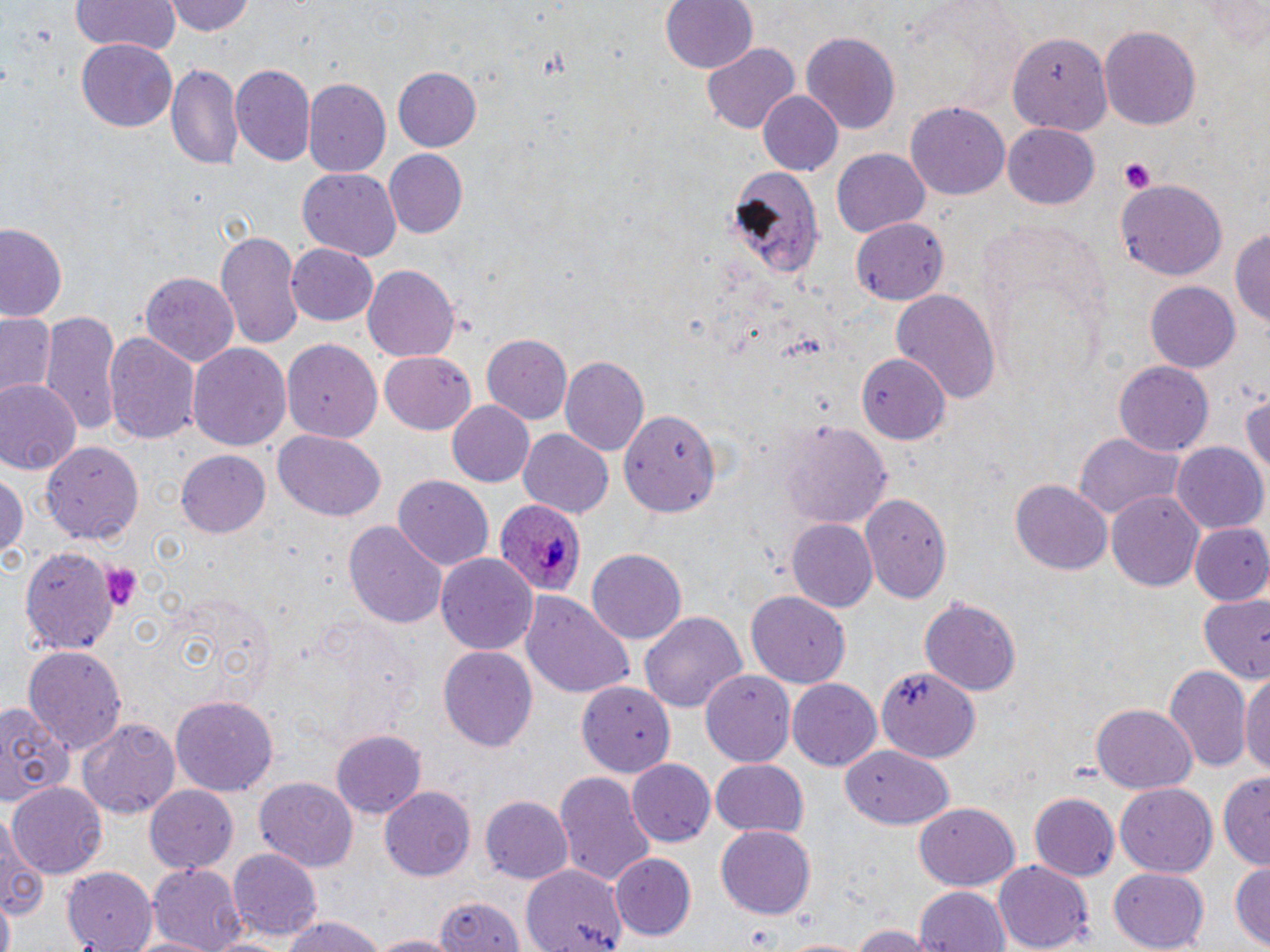
slide-level diagnosis = Plasmodium ovale
field of view = single
uninfected red blood cell locations = approximate bounding boxes as (x1, y1, x2, y2) in pixels: (169, 0, 258, 38), (660, 0, 758, 74), (1199, 0, 1270, 49), (71, 1, 178, 56), (1099, 24, 1202, 131), (800, 31, 901, 135), (1003, 36, 1115, 137), (76, 39, 177, 132), (703, 43, 799, 136), (166, 62, 244, 171), (231, 63, 315, 165), (392, 64, 482, 150), (303, 77, 391, 178), (757, 90, 844, 178), (906, 100, 1009, 200), (1004, 123, 1101, 210), (833, 148, 930, 236), (384, 150, 467, 238), (733, 167, 825, 280), (297, 168, 402, 261), (1114, 177, 1226, 280), (850, 217, 949, 302), (0, 223, 66, 322), (1233, 224, 1270, 337), (215, 229, 304, 349), (287, 243, 379, 327), (360, 262, 461, 363), (140, 271, 240, 367), (1147, 281, 1241, 373), (891, 291, 1000, 409), (41, 309, 119, 435), (1, 312, 58, 400), (55, 313, 178, 439), (104, 331, 200, 450), (481, 334, 573, 423), (282, 337, 382, 442), (187, 342, 291, 452), (379, 352, 476, 434), (562, 355, 651, 456), (855, 356, 949, 446), (1114, 362, 1215, 453), (0, 379, 79, 474), (1241, 379, 1270, 488), (447, 401, 535, 488), (620, 408, 722, 519), (778, 422, 892, 527), (517, 428, 614, 517), (274, 431, 386, 522), (1073, 431, 1189, 520), (40, 440, 144, 546), (1172, 444, 1267, 535), (177, 449, 271, 536), (0, 467, 27, 568), (392, 476, 494, 574), (1010, 478, 1111, 574), (1107, 491, 1204, 592), (861, 494, 952, 604), (787, 519, 877, 614), (345, 522, 446, 629), (1187, 523, 1270, 606), (19, 544, 121, 653), (583, 549, 687, 645), (438, 554, 536, 655), (746, 589, 851, 689), (522, 592, 635, 702), (1195, 592, 1270, 687), (919, 596, 1021, 695), (638, 610, 747, 718), (23, 646, 125, 753), (439, 647, 537, 753), (875, 663, 980, 760), (1164, 665, 1251, 773), (1240, 668, 1270, 783), (701, 671, 796, 766), (787, 678, 880, 772), (577, 679, 676, 775), (169, 696, 279, 796), (0, 698, 72, 809), (1091, 705, 1196, 792), (77, 715, 181, 819), (329, 728, 428, 817), (840, 743, 955, 831), (627, 759, 716, 847), (708, 759, 808, 839), (1217, 768, 1270, 871), (555, 772, 655, 889), (254, 777, 360, 869), (7, 781, 109, 878), (145, 783, 240, 874), (1116, 784, 1218, 877), (380, 786, 477, 880), (1027, 793, 1120, 882), (481, 797, 573, 884), (913, 804, 1020, 891), (0, 815, 47, 927), (716, 826, 817, 918), (228, 848, 322, 940), (614, 854, 694, 939), (1230, 857, 1270, 947), (993, 861, 1094, 951), (522, 862, 628, 952), (148, 863, 246, 949), (59, 865, 154, 948), (1108, 868, 1212, 949), (913, 885, 1009, 952), (433, 890, 524, 952), (1, 898, 16, 952), (279, 915, 385, 952), (848, 922, 926, 952), (130, 933, 217, 952), (369, 933, 451, 952), (773, 935, 870, 952)
platelet locations = approximate bounding boxes as (x1, y1, x2, y2) in pixels: (1118, 157, 1158, 193), (98, 561, 141, 610)
modality = optical microscopy
image size = 1270×952 pixels
Plasmodium ovale-infected red blood cell locations = approximate bounding boxes as (x1, y1, x2, y2) in pixels: (494, 497, 585, 600)
preparation = thin blood film
stain = May-Grünwald-Giemsa
magnification = 1000x